Describe the morphology of the erythrocytes.
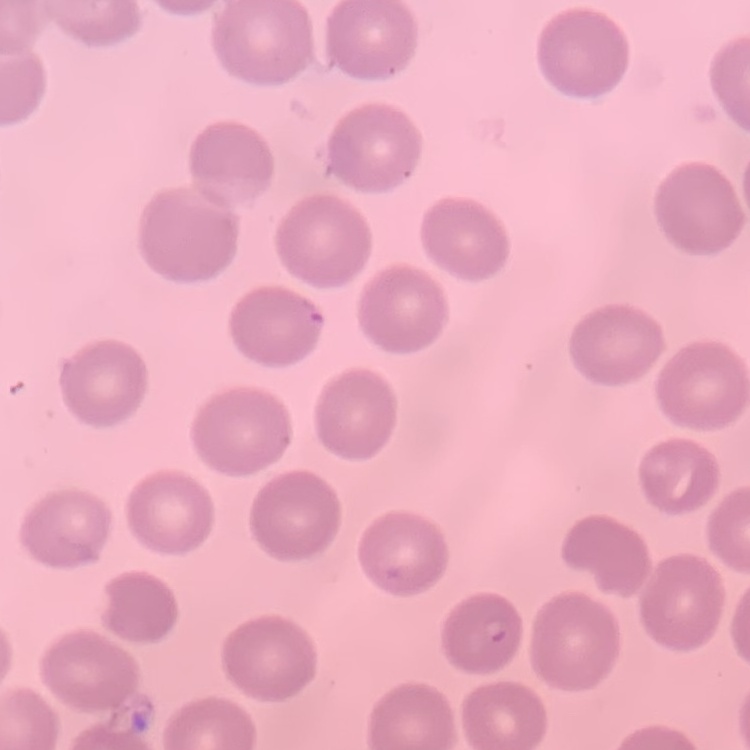
No rouleaux formation.

Stained with either Field's or Giemsa. Thin peripheral smear. Square crop of a larger photomicrograph.